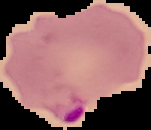
{
  "preparation": "thin blood film",
  "image_type": "segmented cell region with the area outside set to black",
  "image_size": "151×130 pixels",
  "malaria_status": "parasitized"
}